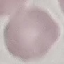 Malaria status: uninfected. Cell patch, automatically extracted from a larger field of view and resized to 64 × 64 pixels. Giemsa stain. Thin blood smear. Acquired by smartphone through the microscope eyepiece.